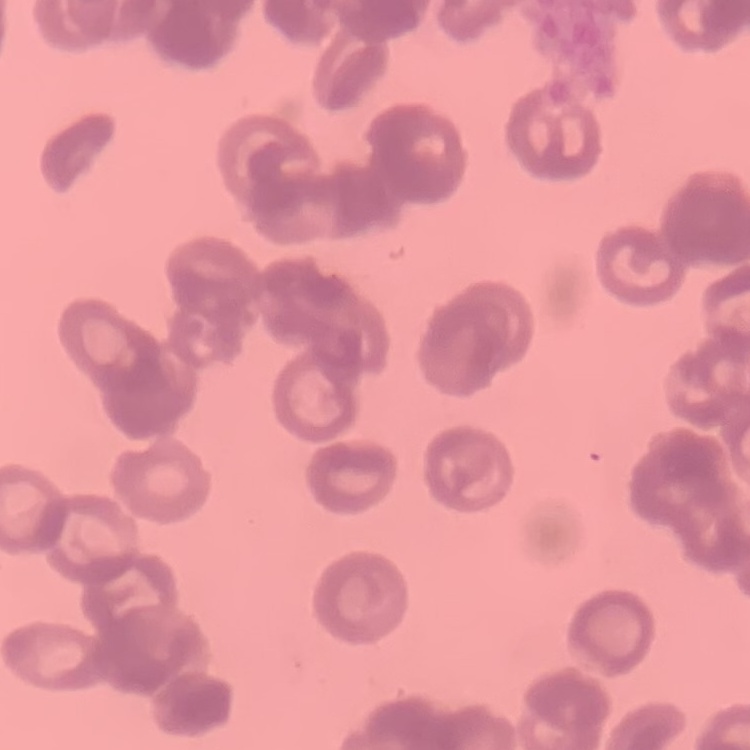
red blood cell morphology = rouleaux formation
stain = Field's or Giemsa
preparation = thin peripheral smear
image type = square crop of a larger photomicrograph